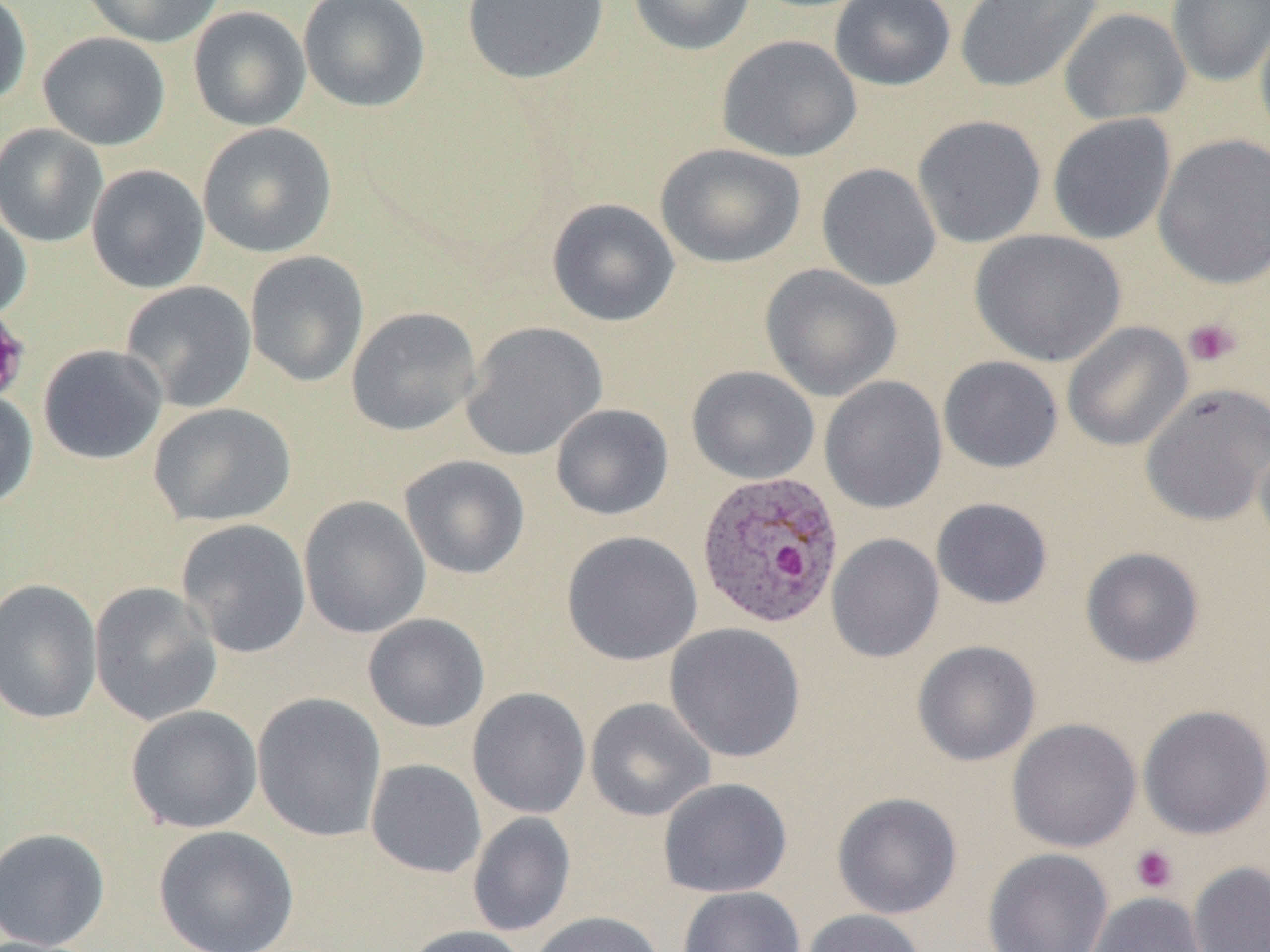 Approximate bounding boxes as (x1,y1)-(x2,y2) corner pairs in pixels. Plasmodium ovale-infected red blood cell locations: (695,469)-(845,630). Platelet locations: (1183,317)-(1242,368), (1130,844)-(1178,893). Uninfected red blood cell locations: (0,0)-(32,108), (80,0)-(226,47), (297,0)-(430,112), (462,0)-(609,85), (628,0)-(757,56), (830,0)-(956,91), (955,0)-(1103,94), (1166,0)-(1270,87), (188,6)-(311,131), (1058,8)-(1191,125), (1254,13)-(1270,149), (38,32)-(171,150), (716,34)-(861,162), (1047,113)-(1176,245), (912,114)-(1047,248), (0,123)-(108,248), (197,123)-(337,259), (1153,133)-(1270,289), (655,142)-(805,268), (817,162)-(941,291), (86,164)-(210,293), (546,198)-(679,327), (0,199)-(32,322), (970,229)-(1127,367), (244,251)-(369,388), (759,264)-(903,401), (120,280)-(257,412), (346,307)-(482,436), (461,321)-(608,461), (1061,322)-(1192,452), (38,344)-(167,465), (938,355)-(1063,473), (686,365)-(819,484), (819,375)-(947,514), (1140,382)-(1270,526), (0,388)-(38,510), (148,402)-(296,526), (550,403)-(674,520), (1254,432)-(1270,556), (399,454)-(531,580), (298,495)-(431,638), (930,497)-(1053,609), (176,518)-(311,659), (561,530)-(702,666), (826,533)-(944,663), (1080,547)-(1205,669), (0,578)-(102,725), (89,582)-(222,726), (363,613)-(490,732), (664,622)-(806,762), (912,640)-(1041,766), (467,687)-(591,819), (252,692)-(386,842), (585,697)-(715,821), (1138,703)-(1270,839), (125,705)-(263,833), (1006,718)-(1142,852), (365,758)-(487,878), (658,778)-(793,898), (832,791)-(963,920), (467,812)-(575,937), (153,825)-(299,952), (0,828)-(111,950), (982,847)-(1114,952), (1187,860)-(1270,952), (677,886)-(806,952), (1085,892)-(1210,952), (799,909)-(927,952), (529,911)-(664,952), (399,925)-(533,952). Slide-level diagnosis: Plasmodium ovale. Image is 1270×952 pixels. 1000x magnification. Single field of view. Thin blood smear. Light microscopy.